Classify this cell by malaria status.
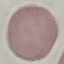
Uninfected.

Automatically extracted cell patch, resized to 64 × 64 pixels. Thin smear of blood. Giemsa-stained preparation. Photographed with a smartphone camera at the microscope eyepiece.